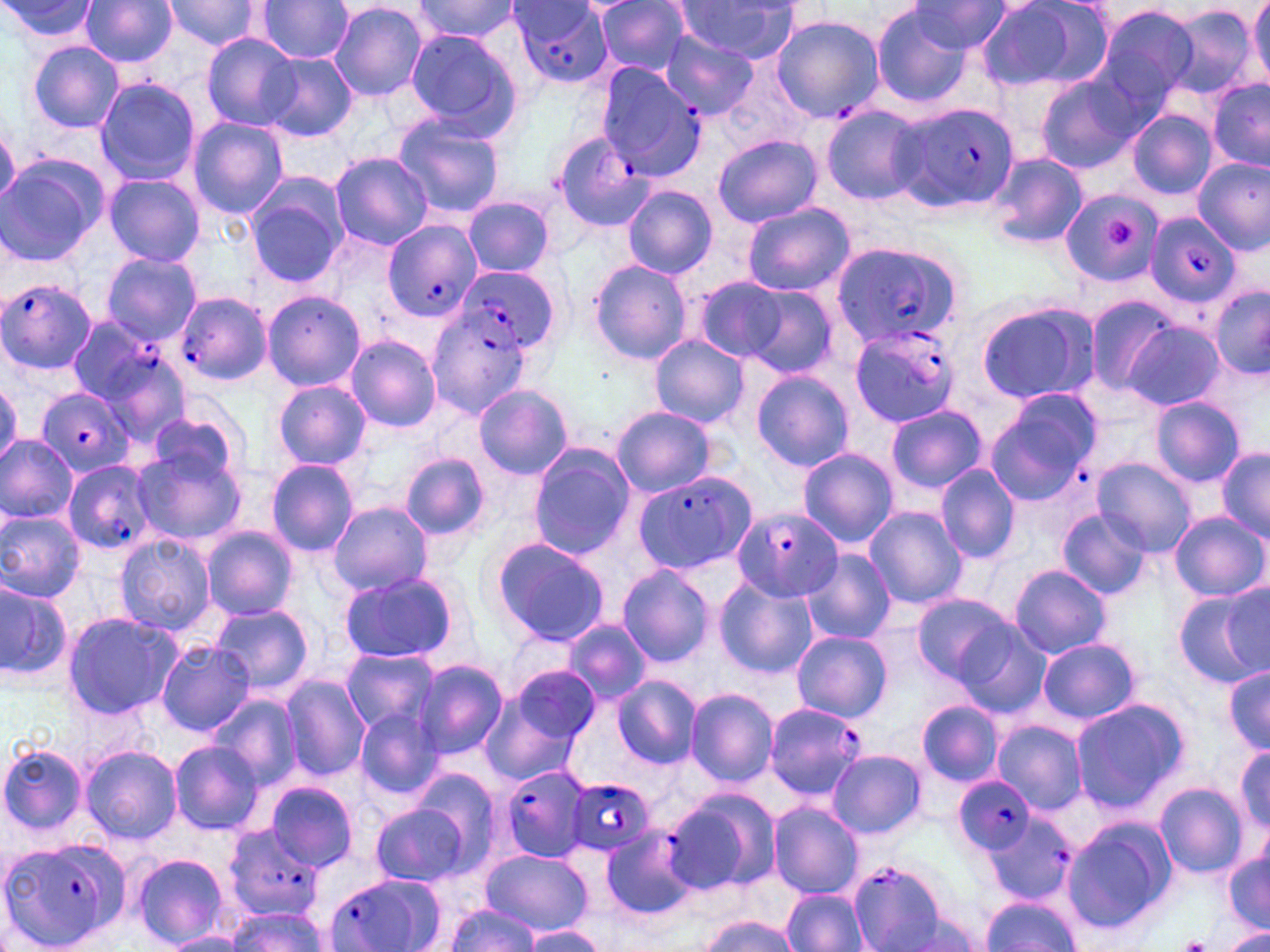

slide-level diagnosis = Plasmodium falciparum
modality = optical microscopy
stain = May-Grünwald-Giemsa
Plasmodium falciparum-infected red blood cell locations (subset) = approximate bounding boxes as [x1, y1, x2, y2] in pixels: [507, 1, 614, 87], [895, 102, 1020, 213], [552, 131, 654, 232], [1147, 213, 1240, 308], [383, 220, 484, 324], [829, 241, 966, 348], [454, 270, 557, 357], [1, 278, 99, 376], [176, 291, 272, 387], [426, 309, 533, 418], [66, 316, 165, 407], [848, 323, 959, 427], [41, 387, 135, 480], [62, 460, 158, 554], [631, 471, 757, 575], [731, 509, 843, 601], [762, 703, 866, 801], [498, 764, 593, 865], [565, 776, 654, 859], [956, 777, 1035, 855], [980, 811, 1078, 907], [225, 824, 327, 921], [600, 828, 698, 920], [1, 837, 132, 950], [846, 860, 953, 952], [323, 871, 446, 952]
field of view = one of a larger specimen
platelet locations = approximate bounding boxes as [x1, y1, x2, y2] in pixels: [1104, 218, 1137, 249], [1175, 935, 1214, 952]
magnification = 1000x
uninfected red blood cell locations (subset) = approximate bounding boxes as [x1, y1, x2, y2] in pixels: [0, 0, 100, 44], [79, 0, 177, 68], [159, 0, 267, 52], [255, 0, 354, 62], [412, 0, 519, 44], [590, 0, 694, 76], [975, 0, 1107, 93], [1248, 0, 1269, 86], [672, 1, 806, 63], [908, 1, 1013, 54], [329, 2, 428, 103], [869, 3, 973, 106], [1094, 3, 1201, 109], [1163, 6, 1258, 102], [771, 14, 884, 122], [403, 29, 521, 136], [659, 29, 759, 119], [201, 32, 299, 131], [27, 40, 124, 134], [260, 53, 357, 142], [1035, 73, 1144, 174], [93, 78, 199, 186], [1208, 78, 1270, 172], [820, 106, 927, 204], [1128, 110, 1215, 200], [391, 114, 506, 218], [187, 118, 288, 219], [713, 134, 821, 228], [330, 152, 433, 249], [986, 153, 1087, 251], [0, 156, 106, 268], [102, 173, 206, 266], [244, 176, 349, 287], [623, 185, 718, 278], [1061, 191, 1163, 287], [464, 196, 557, 278], [740, 202, 854, 296], [101, 251, 201, 346], [589, 258, 693, 365], [693, 278, 789, 361], [1209, 282, 1270, 382], [737, 283, 837, 377], [262, 290, 365, 391], [1083, 295, 1178, 398], [975, 300, 1097, 406], [1122, 320, 1224, 412], [344, 335, 441, 432], [648, 335, 751, 428], [97, 348, 192, 446], [752, 370, 854, 470], [273, 381, 372, 469], [0, 383, 22, 465], [474, 384, 573, 480], [984, 395, 1100, 508], [1150, 398, 1245, 487], [885, 405, 987, 494], [147, 407, 245, 491], [611, 407, 716, 497], [0, 435, 78, 526], [131, 441, 247, 547], [528, 445, 636, 558], [798, 447, 899, 549], [1216, 448, 1270, 543], [402, 453, 489, 541], [1092, 457, 1198, 556], [265, 459, 359, 556], [935, 465, 1020, 564], [326, 502, 433, 597], [864, 506, 968, 610], [1056, 508, 1151, 598], [0, 510, 85, 602], [1170, 511, 1267, 601], [202, 527, 299, 619], [115, 534, 217, 635], [490, 537, 609, 646], [800, 550, 895, 645], [617, 565, 714, 667], [1008, 565, 1112, 658], [337, 571, 461, 665], [714, 577, 817, 678], [0, 579, 72, 680], [1221, 582, 1270, 677], [1174, 590, 1266, 687], [913, 593, 1016, 686], [212, 605, 314, 696], [61, 611, 182, 720], [940, 615, 1049, 719], [564, 619, 652, 703], [792, 630, 892, 721], [1038, 637, 1142, 725], [155, 640, 257, 736], [340, 649, 438, 733], [413, 660, 507, 759], [506, 662, 602, 753], [1224, 665, 1269, 754], [279, 674, 371, 781], [611, 675, 700, 768], [686, 688, 778, 786], [478, 689, 585, 788], [207, 695, 301, 790], [1070, 697, 1188, 810], [916, 700, 1004, 787], [354, 706, 445, 801], [994, 721, 1086, 814], [168, 741, 264, 834], [0, 744, 89, 838], [80, 744, 183, 844], [1234, 744, 1270, 829], [828, 750, 925, 838], [411, 767, 502, 870], [265, 782, 359, 872], [1155, 783, 1248, 878], [661, 787, 778, 897], [768, 802, 864, 898], [371, 805, 469, 886], [1061, 817, 1175, 936], [481, 850, 592, 935], [1224, 850, 1270, 932], [131, 853, 231, 949], [783, 888, 866, 951], [980, 896, 1080, 951], [440, 903, 543, 952], [223, 905, 328, 951], [895, 913, 983, 952], [699, 916, 800, 952], [519, 927, 606, 951], [1223, 929, 1270, 952], [160, 933, 244, 952]
image size = 1270×952 pixels
preparation = thin blood smear